Locate every blood parasite and identify its species.
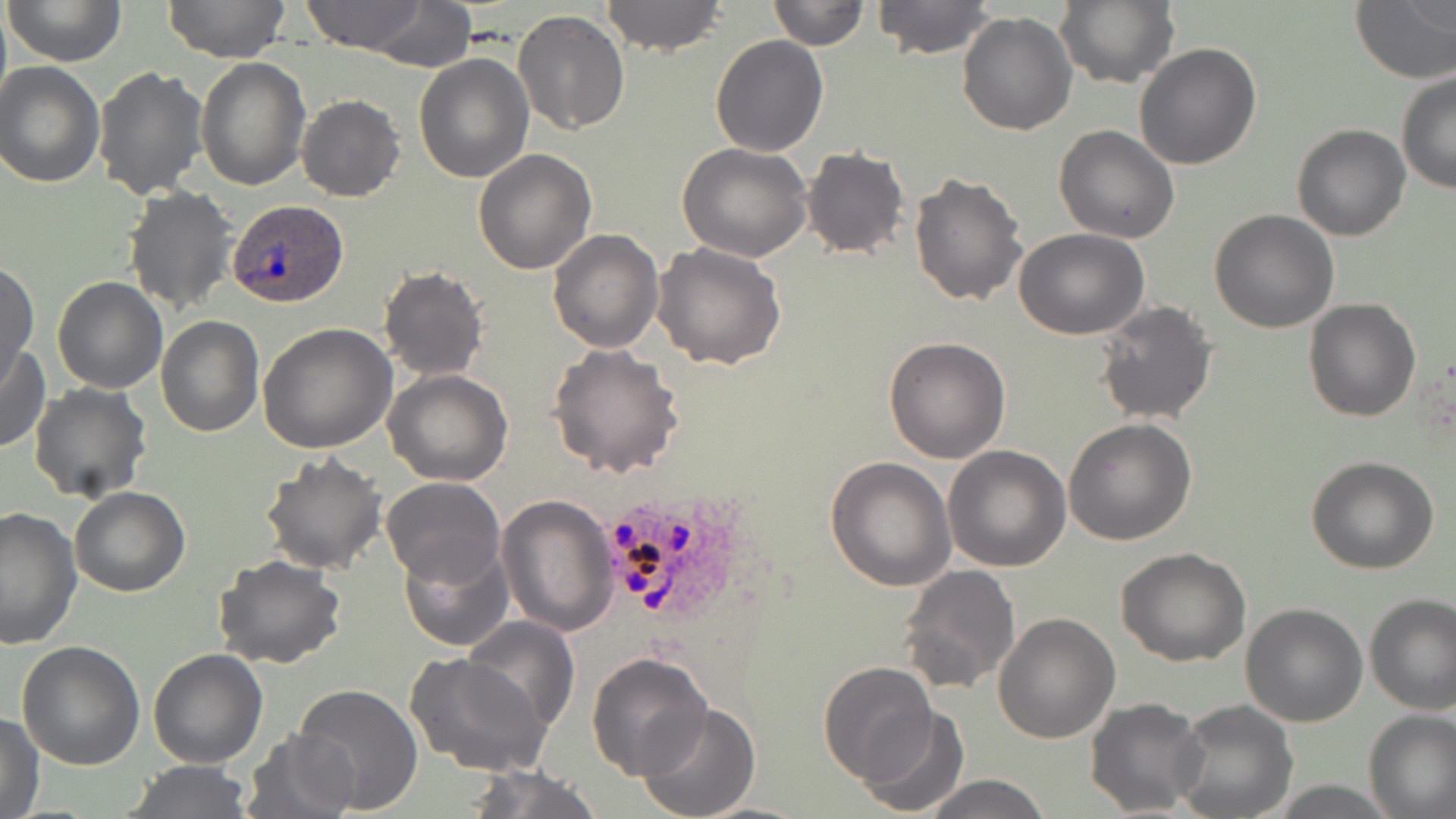
Approximate bounding boxes as [x1, y1, x2, y2] in pixels.
Plasmodium ovale-infected red blood cells: [227, 201, 345, 308], [603, 496, 740, 625].
No Plasmodium falciparum, Plasmodium malariae, Plasmodium vivax, Babesia divergens, or Trypanosoma brucei observed.

Summary:
  - Uninfected red blood cell locations: [4, 0, 126, 68], [163, 0, 291, 66], [300, 0, 432, 53], [601, 0, 727, 56], [765, 0, 869, 49], [871, 0, 995, 57], [1054, 0, 1179, 88], [1349, 0, 1456, 84], [347, 3, 477, 69], [513, 9, 630, 136], [956, 11, 1077, 136], [711, 34, 827, 155], [1133, 42, 1261, 170], [413, 52, 532, 183], [195, 57, 309, 190], [0, 61, 104, 187], [92, 66, 209, 201], [1397, 70, 1456, 194], [297, 94, 405, 202], [1054, 124, 1181, 243], [1291, 124, 1411, 241], [678, 142, 813, 261], [800, 146, 912, 260], [474, 149, 597, 275], [910, 171, 1029, 307], [123, 185, 238, 317], [1209, 209, 1340, 333], [548, 227, 664, 353], [1013, 229, 1150, 340], [651, 242, 786, 371], [0, 260, 37, 382], [377, 267, 487, 381], [51, 275, 168, 395], [1303, 298, 1422, 423], [1093, 300, 1217, 425], [156, 317, 265, 438], [257, 322, 397, 454], [883, 336, 1012, 464], [0, 343, 48, 452], [547, 344, 685, 478], [383, 368, 513, 485], [28, 384, 150, 503], [1064, 419, 1196, 544], [943, 446, 1072, 571], [258, 451, 387, 574], [1306, 454, 1439, 574], [825, 456, 955, 592], [381, 476, 505, 590], [69, 486, 192, 597], [496, 494, 618, 635], [0, 505, 81, 650], [396, 542, 513, 653], [1116, 545, 1251, 667], [213, 555, 345, 671], [896, 564, 1021, 696], [1363, 593, 1456, 713], [1240, 603, 1368, 727], [993, 611, 1120, 743], [461, 615, 580, 736], [16, 641, 146, 770], [147, 648, 268, 768], [586, 652, 713, 777], [404, 653, 554, 780], [820, 661, 939, 785], [291, 684, 423, 811], [1085, 697, 1209, 817], [1170, 699, 1298, 819], [636, 701, 763, 819], [855, 707, 968, 816], [1364, 708, 1456, 817], [1, 710, 44, 818], [242, 729, 361, 819], [124, 759, 255, 817], [459, 762, 603, 819], [919, 774, 1053, 818]
  - Slide-level diagnosis: Plasmodium ovale
  - Field of view: single
  - Stain: May-Grünwald-Giemsa
  - Magnification: 1000x
  - Image size: 1456×819 pixels
  - Modality: optical microscopy
  - Preparation: thin blood smear